Report the malaria status of this cell.
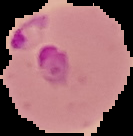

Parasitized.

image size = 133×136 pixels
image type = segmented cell region on a black background
preparation = thin blood smear